Name the parasite shown.
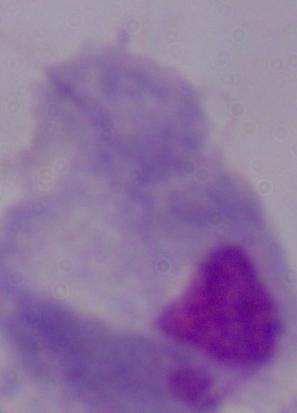
A trichomonad.

Photomicrograph. 1000x magnification.